Evaluate for malaria.
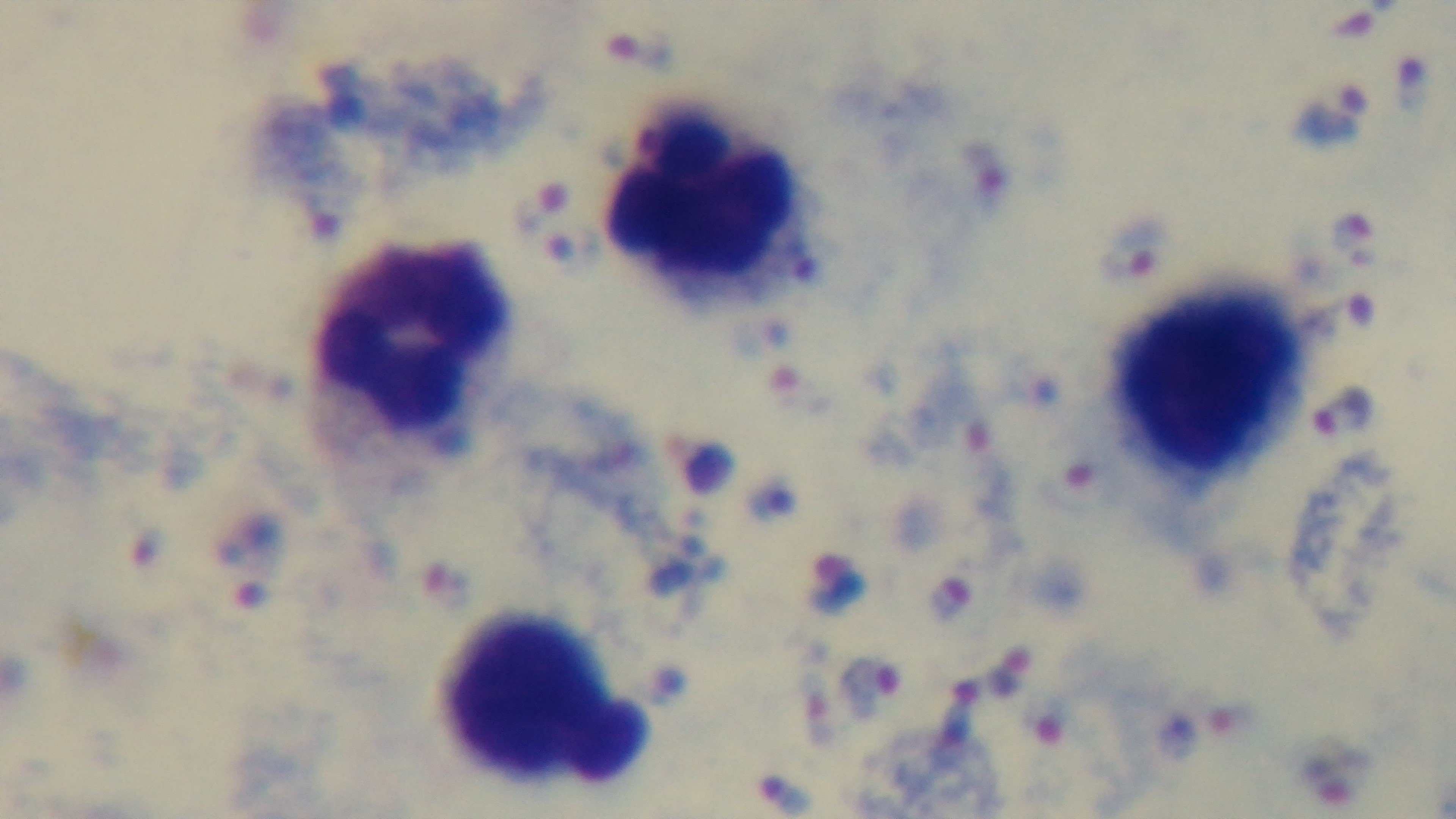
Positive.

preparation = thick smear
capture = mounted 4K digital camera
objective = 100x oil immersion
field of view = single
modality = light microscopy
stain = Giemsa